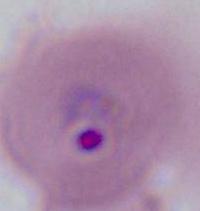
identification = Plasmodium
modality = micrograph
magnification = 400x or 1000x